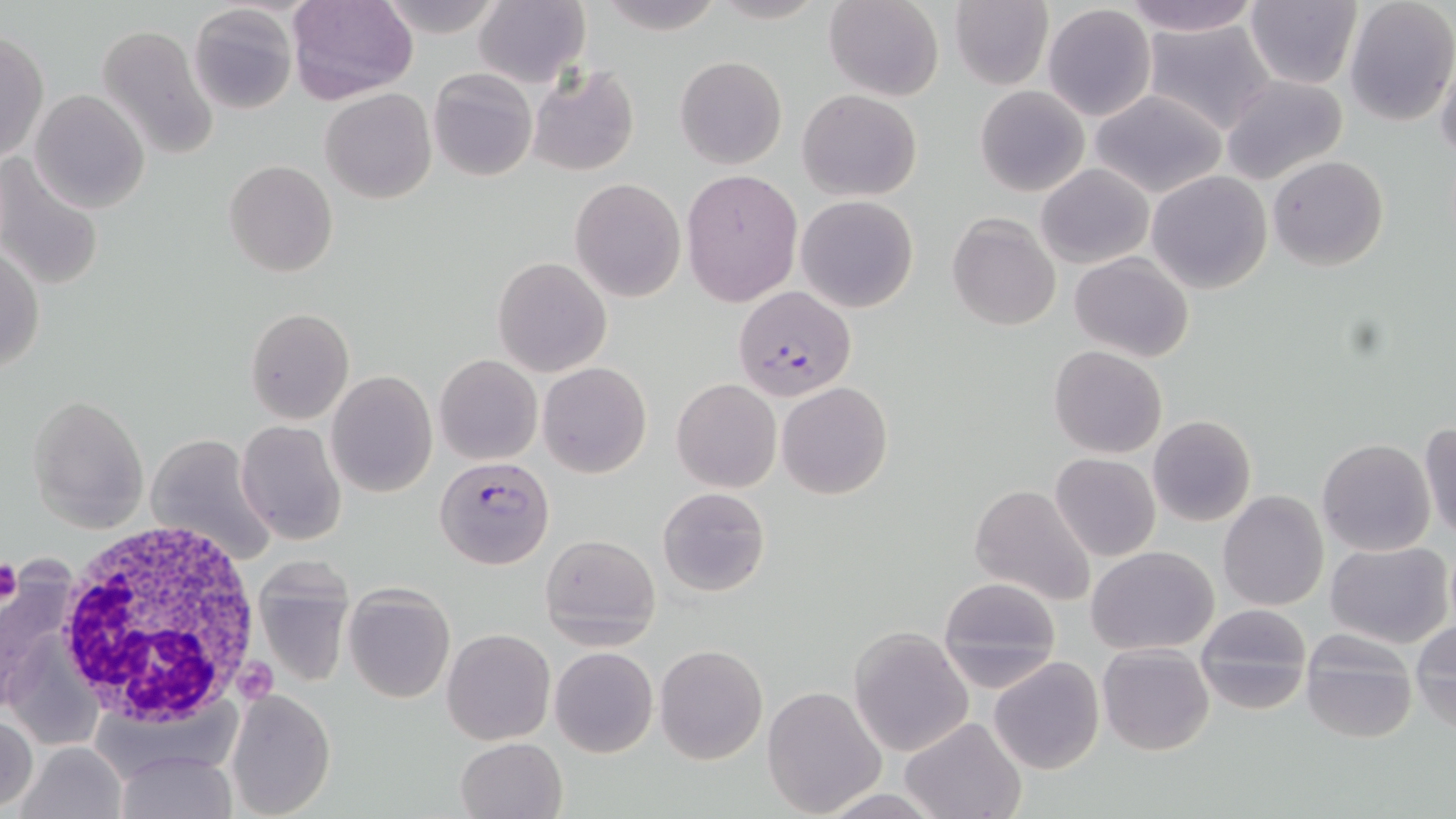

Summary:
  - Coordinate format: approximate bounding boxes as (x1, y1, x2, y2) in pixels
  - Platelet locations: (0, 559, 24, 606), (237, 663, 277, 701)
  - White blood cell locations: (55, 517, 270, 729)
  - Uninfected red blood cell locations: (286, 0, 417, 105), (372, 0, 507, 36), (589, 0, 729, 34), (824, 0, 944, 101), (1117, 0, 1266, 37), (1245, 0, 1363, 90), (472, 1, 589, 87), (948, 1, 1053, 89), (1345, 2, 1455, 127), (188, 5, 296, 113), (1042, 5, 1156, 123), (1140, 18, 1276, 135), (96, 24, 218, 160), (1, 30, 47, 164), (1436, 53, 1456, 167), (674, 56, 788, 171), (527, 64, 640, 175), (429, 69, 536, 182), (1219, 74, 1349, 185), (976, 85, 1089, 197), (320, 88, 436, 204), (31, 89, 150, 213), (798, 89, 923, 202), (1088, 89, 1229, 198), (0, 152, 105, 290), (1268, 155, 1388, 271), (223, 159, 338, 277), (1036, 163, 1154, 269), (681, 168, 802, 308), (1146, 170, 1272, 294), (570, 179, 686, 302), (795, 195, 920, 314), (947, 212, 1061, 330), (1, 242, 44, 378), (1071, 252, 1195, 362), (493, 256, 612, 376), (246, 308, 354, 424), (1049, 346, 1166, 458), (434, 354, 541, 464), (538, 361, 652, 478), (326, 370, 438, 498), (670, 378, 781, 493), (776, 382, 893, 501), (29, 395, 149, 532), (1148, 415, 1256, 527), (236, 420, 345, 545), (1420, 420, 1456, 544), (145, 434, 276, 565), (1317, 437, 1436, 556), (1050, 453, 1160, 562), (969, 483, 1095, 607), (657, 485, 771, 597), (1217, 491, 1329, 612), (540, 534, 660, 650), (1326, 541, 1454, 649), (1087, 545, 1220, 654), (252, 556, 356, 690), (0, 570, 85, 718), (936, 577, 1061, 690), (343, 584, 456, 704), (957, 599, 1090, 755), (1196, 604, 1312, 714), (1412, 619, 1456, 732), (850, 625, 975, 757), (443, 628, 556, 745), (1302, 631, 1418, 746), (1098, 643, 1214, 756), (654, 644, 767, 764), (549, 646, 658, 756), (989, 656, 1105, 774), (760, 685, 888, 816), (226, 686, 336, 816), (0, 712, 39, 811), (901, 716, 1024, 819), (455, 737, 568, 819), (14, 742, 127, 819), (112, 749, 236, 819)
  - Plasmodium falciparum-infected red blood cell locations: (731, 286, 857, 402), (436, 455, 554, 568)
  - Slide-level diagnosis: Plasmodium falciparum
  - Magnification: 1000x
  - Preparation: thin blood smear
  - Stain: May-Grünwald-Giemsa
  - Image size: 1456×819 pixels
  - Field of view: one of a larger specimen
  - Modality: optical microscopy